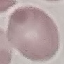
result: no malaria parasites detected
stain: Giemsa
preparation: thin blood smear
capture: smartphone camera at the microscope eyepiece
image_type: automatically extracted cell patch, resized to 64 × 64 pixels